Evaluate for malaria.
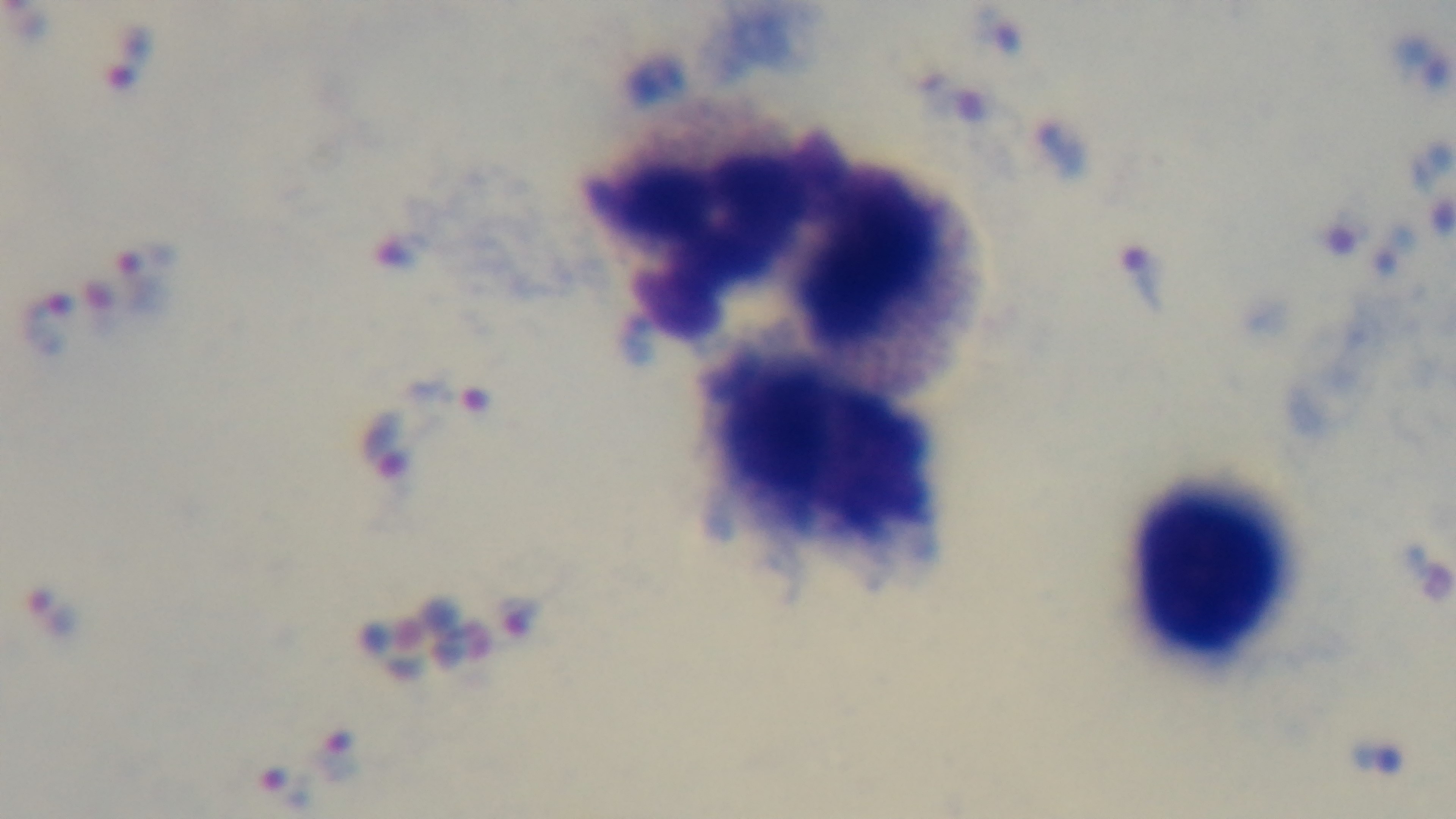
Infected.

objective = 100x oil immersion
stain = Giemsa
preparation = thick
field of view = one from the slide
capture = mounted 4K digital camera
modality = light microscopy